Locate every blood parasite and identify its species.
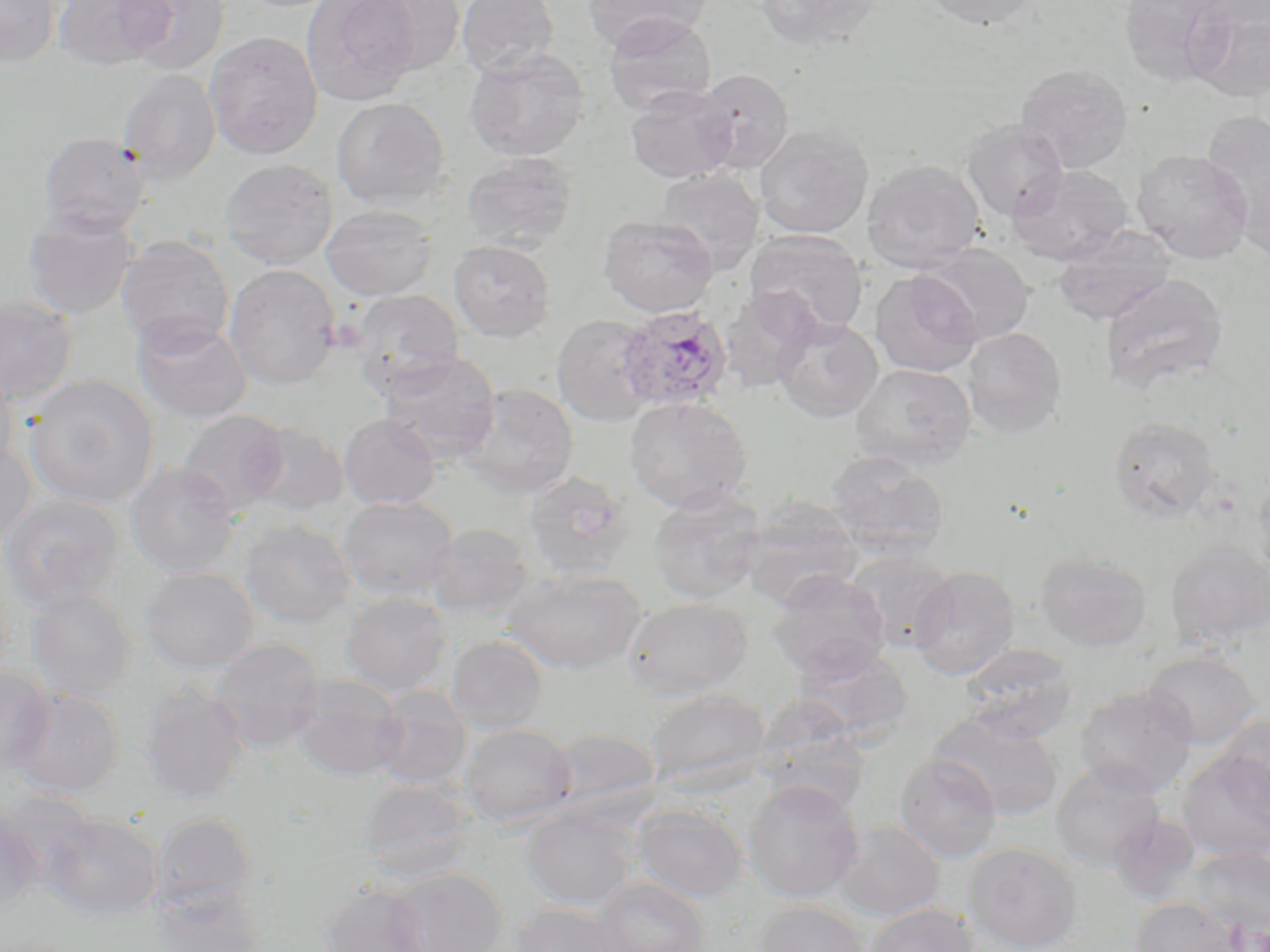

Approximate bounding boxes as (x1, y1, x2, y2) in pixels.
Plasmodium ovale-infected red blood cells: (615, 305, 734, 413).
No Plasmodium falciparum, Plasmodium malariae, Plasmodium vivax, Babesia divergens, or Trypanosoma brucei observed.

slide-level diagnosis = Plasmodium ovale
platelet locations = approximate bounding boxes as (x1, y1, x2, y2) in pixels: (326, 316, 366, 353)
preparation = thin blood film
field of view = one of a larger specimen
modality = optical microscopy
magnification = 1000x
stain = May-Grünwald-Giemsa
uninfected red blood cell locations = approximate bounding boxes as (x1, y1, x2, y2) in pixels: (0, 0, 61, 67), (52, 0, 170, 69), (118, 0, 230, 76), (301, 0, 420, 106), (457, 0, 559, 79), (581, 0, 712, 52), (756, 0, 886, 51), (922, 0, 1041, 30), (1119, 0, 1234, 86), (359, 1, 467, 74), (1187, 1, 1270, 102), (602, 12, 717, 116), (205, 31, 323, 159), (464, 47, 589, 162), (1015, 63, 1134, 173), (118, 68, 221, 184), (693, 68, 795, 173), (625, 86, 737, 183), (331, 97, 450, 209), (1203, 112, 1270, 248), (962, 119, 1069, 222), (754, 124, 874, 239), (38, 133, 151, 236), (1131, 149, 1254, 263), (462, 152, 578, 251), (220, 158, 338, 269), (861, 159, 985, 272), (1007, 164, 1133, 265), (653, 169, 763, 273), (321, 205, 437, 301), (21, 208, 138, 319), (598, 215, 718, 318), (1052, 226, 1176, 326), (744, 229, 869, 337), (115, 235, 235, 352), (448, 239, 556, 342), (920, 242, 1034, 345), (224, 264, 340, 390), (869, 269, 983, 377), (1099, 273, 1229, 397), (719, 289, 820, 393), (351, 290, 465, 395), (0, 296, 78, 404), (551, 313, 661, 427), (131, 315, 252, 423), (772, 317, 883, 422), (961, 327, 1067, 438), (378, 350, 500, 464), (850, 363, 977, 468), (0, 365, 18, 475), (25, 374, 159, 508), (455, 383, 578, 499), (623, 395, 753, 513), (178, 409, 289, 516), (339, 414, 440, 510), (1108, 416, 1221, 522), (245, 422, 349, 516), (0, 440, 36, 551), (825, 449, 949, 557), (126, 462, 241, 577), (1253, 466, 1270, 579), (524, 471, 634, 581), (647, 487, 767, 605), (0, 494, 124, 610), (740, 496, 864, 607), (338, 497, 458, 601), (240, 519, 355, 628), (427, 523, 534, 619), (1166, 540, 1270, 648), (1035, 549, 1152, 651), (845, 550, 957, 652), (909, 565, 1020, 679), (140, 566, 259, 672), (503, 568, 646, 674), (766, 570, 891, 679), (25, 589, 136, 699), (341, 592, 452, 696), (622, 597, 753, 699), (445, 635, 549, 734), (209, 638, 325, 752), (791, 642, 914, 743), (960, 644, 1078, 742), (1142, 650, 1261, 749), (0, 667, 55, 774), (289, 675, 407, 782), (140, 684, 250, 803), (1074, 685, 1197, 797), (8, 686, 124, 797), (371, 686, 472, 791), (648, 688, 771, 794), (754, 703, 872, 814), (929, 711, 1064, 820), (1216, 713, 1270, 821), (460, 723, 576, 827), (545, 728, 661, 816), (1177, 751, 1270, 861), (894, 753, 1002, 862), (1051, 762, 1166, 869), (743, 779, 865, 902), (358, 780, 475, 883), (631, 803, 748, 903), (522, 807, 637, 909), (0, 810, 41, 915), (150, 812, 259, 913), (1109, 812, 1201, 903), (41, 813, 163, 922), (833, 820, 945, 921), (964, 841, 1083, 952), (1182, 846, 1269, 935), (385, 868, 508, 952), (592, 878, 710, 952), (320, 881, 433, 952), (150, 884, 266, 952), (1131, 898, 1241, 952), (754, 900, 869, 952), (863, 902, 979, 952), (509, 903, 624, 952)
image size = 1270×952 pixels